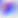
magnification = 400x
modality = micrograph
identification = Toxoplasma gondii